Locate every blood parasite and identify its species.
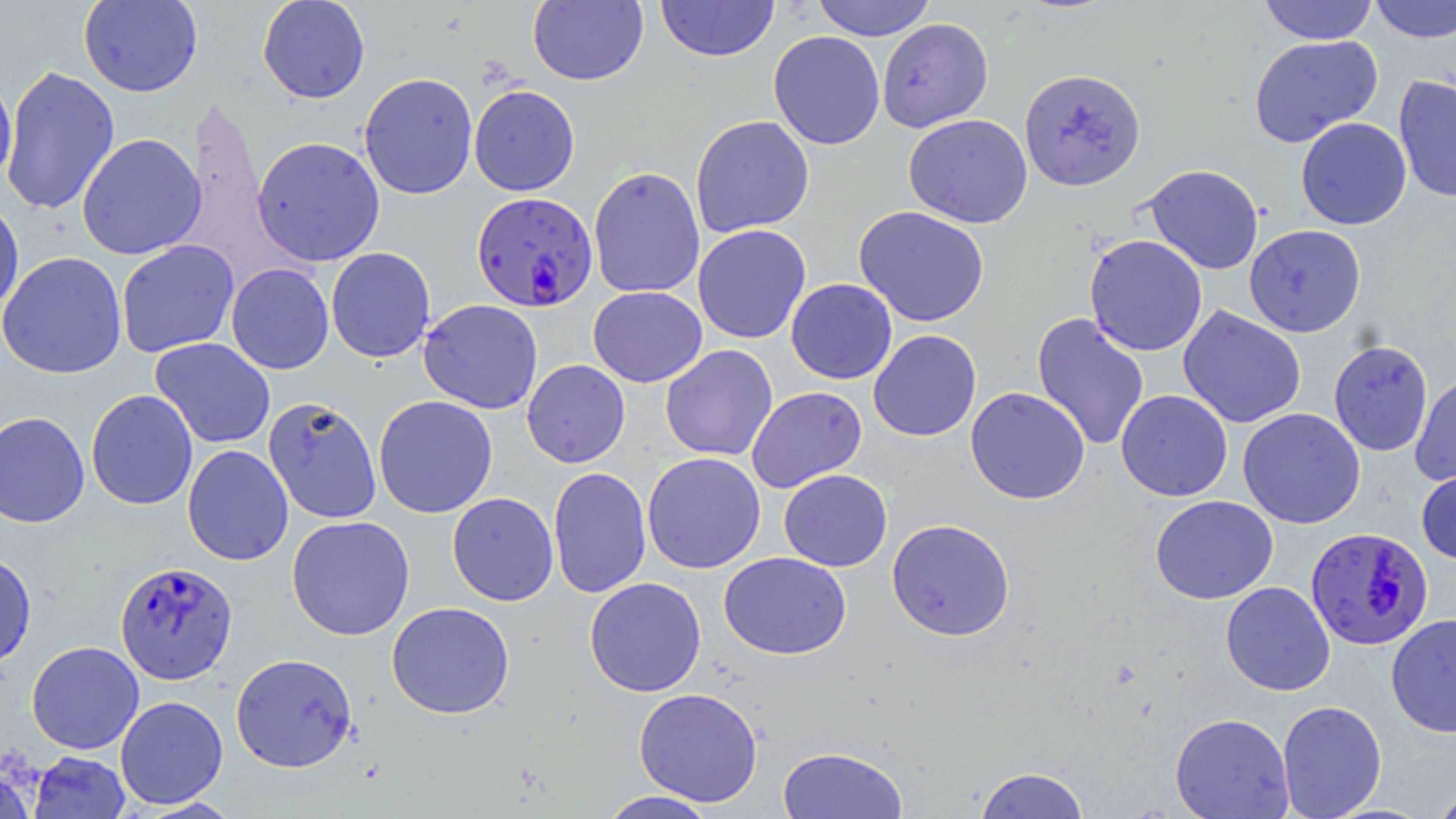

Approximate bounding boxes as (x1, y1, x2, y2) in pixels.
Plasmodium falciparum-infected red blood cells: (471, 191, 597, 312), (1305, 527, 1434, 651), (114, 560, 238, 683).
No Plasmodium ovale, Plasmodium malariae, Plasmodium vivax, Babesia divergens, or Trypanosoma brucei observed.

{
  "slide_level_diagnosis": "Plasmodium falciparum",
  "modality": "optical microscopy",
  "stain": "May-Grünwald-Giemsa",
  "magnification": "1000x",
  "preparation": "thin blood smear",
  "field_of_view": "single",
  "uninfected_red_blood_cell_locations": "approximate bounding boxes as (x1, y1, x2, y2) in pixels: (78, 0, 203, 97), (257, 0, 370, 104), (528, 0, 648, 86), (655, 0, 779, 62), (811, 0, 936, 40), (1258, 0, 1379, 44), (1368, 0, 1456, 43), (876, 18, 993, 132), (768, 31, 885, 150), (1248, 35, 1383, 147), (2, 65, 120, 216), (1019, 68, 1146, 191), (0, 70, 17, 186), (358, 72, 478, 200), (1393, 74, 1456, 204), (469, 85, 580, 196), (903, 114, 1032, 228), (690, 115, 815, 237), (1295, 117, 1412, 230), (77, 133, 206, 260), (251, 136, 385, 266), (1142, 164, 1264, 274), (588, 166, 705, 299), (0, 196, 24, 321), (853, 206, 990, 327), (692, 224, 812, 344), (1244, 224, 1367, 337), (1084, 234, 1208, 356), (116, 240, 239, 358), (325, 247, 435, 363), (0, 252, 127, 379), (226, 263, 334, 374), (786, 278, 897, 384), (588, 285, 707, 387), (418, 299, 543, 414), (1178, 305, 1306, 428), (1031, 312, 1150, 451), (868, 330, 981, 441), (149, 338, 276, 449), (1328, 340, 1433, 456), (660, 344, 777, 461), (522, 359, 630, 468), (1410, 372, 1456, 486), (746, 386, 867, 493), (965, 387, 1090, 504), (86, 389, 198, 510), (1115, 389, 1233, 501), (373, 395, 498, 518), (263, 396, 382, 524), (1237, 408, 1365, 529), (0, 411, 90, 527), (182, 444, 294, 565), (642, 452, 766, 574), (1416, 465, 1456, 564), (548, 467, 652, 598), (779, 469, 892, 571), (447, 492, 559, 606), (1150, 495, 1278, 604), (287, 515, 415, 640), (886, 518, 1016, 641), (0, 551, 37, 670), (719, 552, 851, 659), (584, 577, 707, 697), (1220, 581, 1335, 696), (386, 602, 514, 718), (1386, 613, 1456, 738), (27, 641, 144, 754), (231, 653, 358, 773), (633, 687, 763, 806), (115, 695, 228, 809), (1277, 700, 1387, 818), (1169, 712, 1294, 819), (777, 746, 908, 818), (29, 751, 131, 819), (973, 766, 1091, 819), (0, 767, 37, 819), (1430, 784, 1456, 819), (599, 790, 717, 818)",
  "image_size": "1456×819 pixels"
}